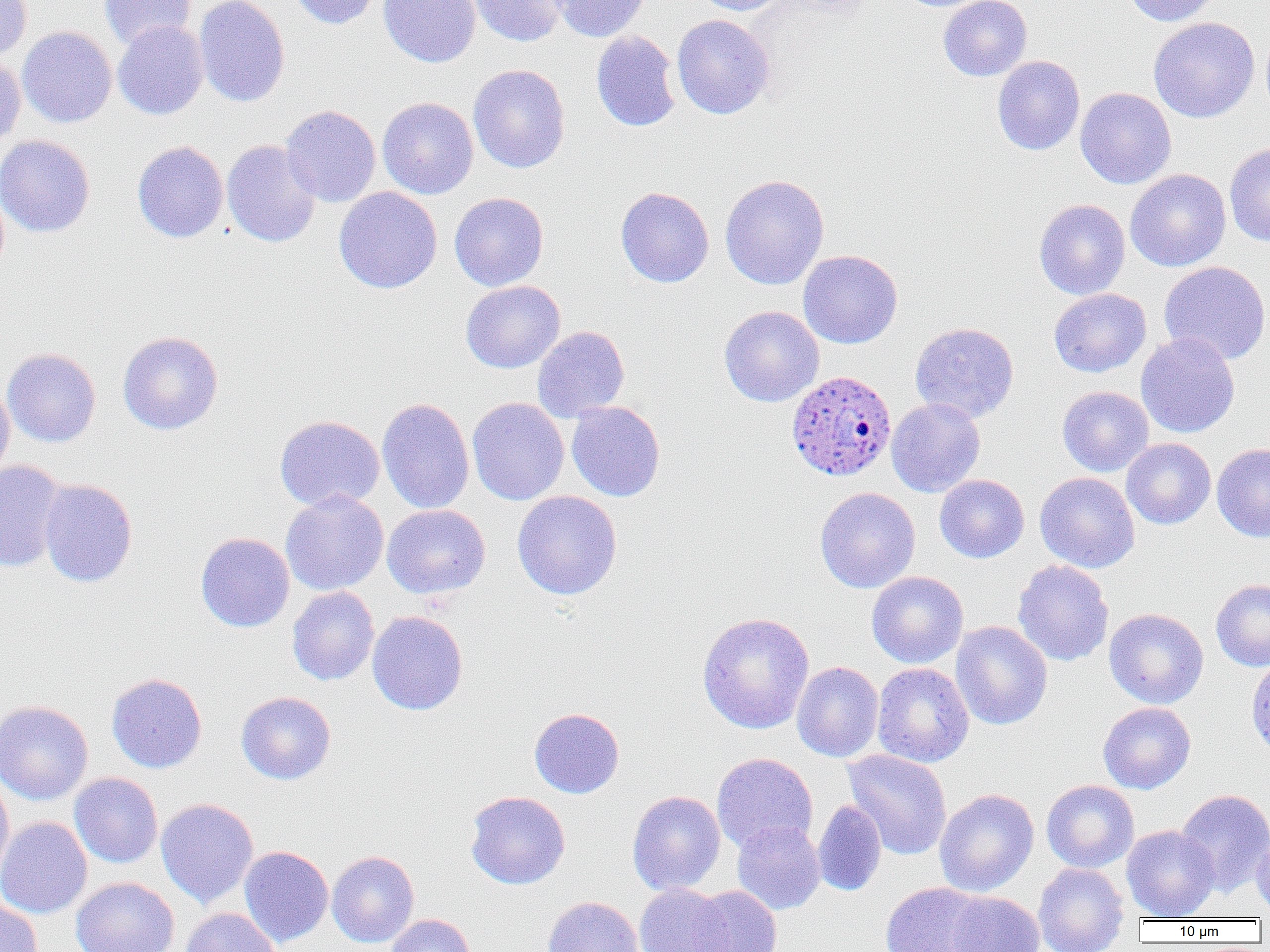

Summary:
  - Coordinate format: approximate bounding boxes as named x1/y1/x2/y2 corners in pixels
  - Plasmodium ovale-infected red blood cell locations: (x1=786, y1=370, x2=897, y2=481)
  - Uninfected red blood cell locations: (x1=0, y1=0, x2=32, y2=60), (x1=98, y1=0, x2=197, y2=50), (x1=194, y1=0, x2=290, y2=107), (x1=289, y1=0, x2=383, y2=29), (x1=379, y1=0, x2=482, y2=67), (x1=468, y1=0, x2=569, y2=47), (x1=551, y1=0, x2=651, y2=42), (x1=690, y1=0, x2=789, y2=15), (x1=938, y1=0, x2=1032, y2=81), (x1=1123, y1=0, x2=1223, y2=26), (x1=672, y1=14, x2=775, y2=119), (x1=1148, y1=17, x2=1260, y2=123), (x1=113, y1=20, x2=209, y2=120), (x1=17, y1=26, x2=117, y2=128), (x1=590, y1=30, x2=681, y2=132), (x1=0, y1=55, x2=26, y2=151), (x1=992, y1=55, x2=1085, y2=155), (x1=468, y1=64, x2=570, y2=173), (x1=1075, y1=87, x2=1176, y2=189), (x1=377, y1=97, x2=478, y2=199), (x1=281, y1=105, x2=381, y2=207), (x1=0, y1=134, x2=95, y2=237), (x1=221, y1=139, x2=321, y2=248), (x1=132, y1=141, x2=229, y2=243), (x1=1224, y1=142, x2=1270, y2=246), (x1=1125, y1=169, x2=1231, y2=272), (x1=719, y1=174, x2=829, y2=290), (x1=333, y1=186, x2=442, y2=294), (x1=615, y1=187, x2=714, y2=287), (x1=449, y1=192, x2=549, y2=291), (x1=1034, y1=199, x2=1130, y2=300), (x1=798, y1=250, x2=903, y2=349), (x1=1159, y1=261, x2=1270, y2=365), (x1=460, y1=280, x2=566, y2=373), (x1=1048, y1=288, x2=1151, y2=377), (x1=718, y1=305, x2=824, y2=407), (x1=909, y1=322, x2=1019, y2=424), (x1=532, y1=326, x2=630, y2=423), (x1=117, y1=331, x2=223, y2=435), (x1=1135, y1=332, x2=1240, y2=438), (x1=2, y1=348, x2=101, y2=447), (x1=0, y1=378, x2=15, y2=482), (x1=1057, y1=386, x2=1154, y2=477), (x1=377, y1=397, x2=475, y2=514), (x1=467, y1=397, x2=569, y2=506), (x1=886, y1=398, x2=986, y2=497), (x1=566, y1=401, x2=666, y2=502), (x1=274, y1=415, x2=385, y2=512), (x1=1121, y1=438, x2=1216, y2=529), (x1=1212, y1=443, x2=1270, y2=541), (x1=0, y1=461, x2=68, y2=572), (x1=1035, y1=472, x2=1139, y2=573), (x1=934, y1=474, x2=1029, y2=563), (x1=38, y1=479, x2=137, y2=587), (x1=814, y1=487, x2=920, y2=593), (x1=280, y1=490, x2=389, y2=595), (x1=512, y1=491, x2=622, y2=600), (x1=382, y1=504, x2=491, y2=599), (x1=195, y1=532, x2=295, y2=632), (x1=1012, y1=559, x2=1113, y2=666), (x1=867, y1=571, x2=968, y2=668), (x1=1210, y1=578, x2=1270, y2=671), (x1=287, y1=586, x2=380, y2=686), (x1=1104, y1=608, x2=1209, y2=709), (x1=367, y1=611, x2=468, y2=715), (x1=696, y1=611, x2=815, y2=734), (x1=951, y1=621, x2=1053, y2=730), (x1=1246, y1=655, x2=1270, y2=758), (x1=792, y1=661, x2=884, y2=762), (x1=872, y1=663, x2=973, y2=768), (x1=106, y1=672, x2=207, y2=773), (x1=236, y1=691, x2=336, y2=785), (x1=0, y1=700, x2=93, y2=805), (x1=1097, y1=702, x2=1196, y2=794), (x1=529, y1=708, x2=625, y2=798), (x1=843, y1=749, x2=952, y2=860), (x1=711, y1=753, x2=818, y2=854), (x1=69, y1=772, x2=163, y2=868), (x1=0, y1=775, x2=14, y2=882), (x1=1041, y1=780, x2=1139, y2=873), (x1=934, y1=788, x2=1039, y2=897), (x1=1175, y1=788, x2=1270, y2=896), (x1=627, y1=790, x2=726, y2=896), (x1=465, y1=791, x2=570, y2=889), (x1=156, y1=798, x2=258, y2=907), (x1=812, y1=800, x2=887, y2=896), (x1=0, y1=816, x2=92, y2=919), (x1=732, y1=820, x2=825, y2=914), (x1=1121, y1=825, x2=1220, y2=921), (x1=1251, y1=828, x2=1269, y2=919), (x1=239, y1=845, x2=334, y2=947), (x1=327, y1=850, x2=419, y2=948), (x1=1033, y1=862, x2=1129, y2=952), (x1=71, y1=876, x2=178, y2=952), (x1=880, y1=882, x2=990, y2=951), (x1=634, y1=883, x2=731, y2=952), (x1=690, y1=886, x2=782, y2=952), (x1=946, y1=891, x2=1044, y2=952), (x1=542, y1=896, x2=643, y2=952), (x1=0, y1=899, x2=42, y2=952), (x1=180, y1=907, x2=282, y2=952), (x1=385, y1=914, x2=476, y2=952)
  - Slide-level diagnosis: Plasmodium ovale
  - Preparation: thin blood smear
  - Magnification: 1000x
  - Modality: optical microscopy
  - Field of view: single
  - Image size: 1270×952 pixels